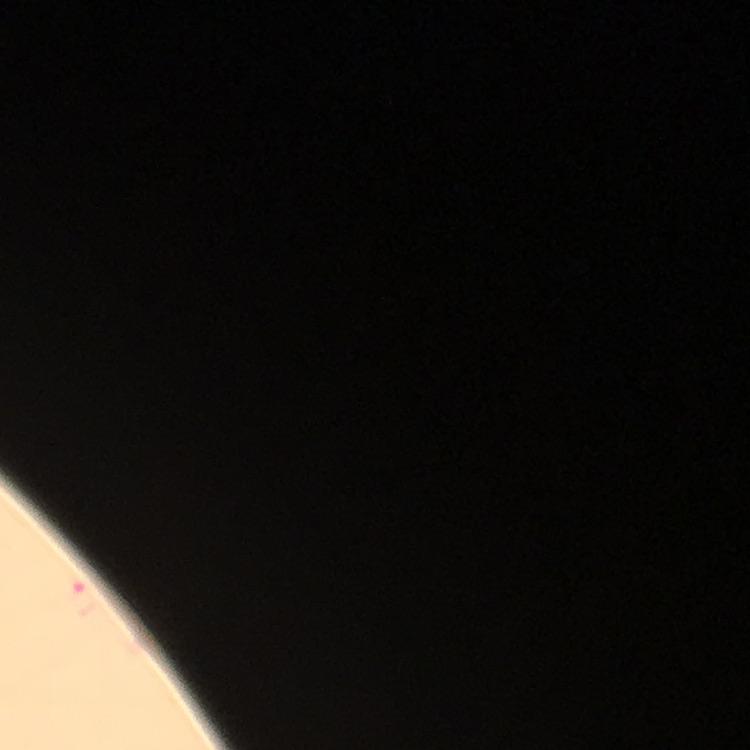
Approximate centers as [x, y] in pixels.
Summary:
  - Malaria parasite locations: [82, 599]
  - Magnification: 100x
  - Immersion oil: applied
  - Context: from a diagnostic examination for malaria
  - Image size: 750×750 pixels
  - Preparation: thick blood smear
  - Cropped from: one field of view
  - Capture: smartphone camera through the microscope
  - Stain: Giemsa